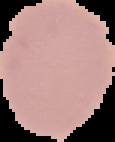
image_type: cell region segmented out of the field of view; surrounding area masked to black
image_size: 115×142 pixels
result: no malaria parasites detected
preparation: thin blood smear